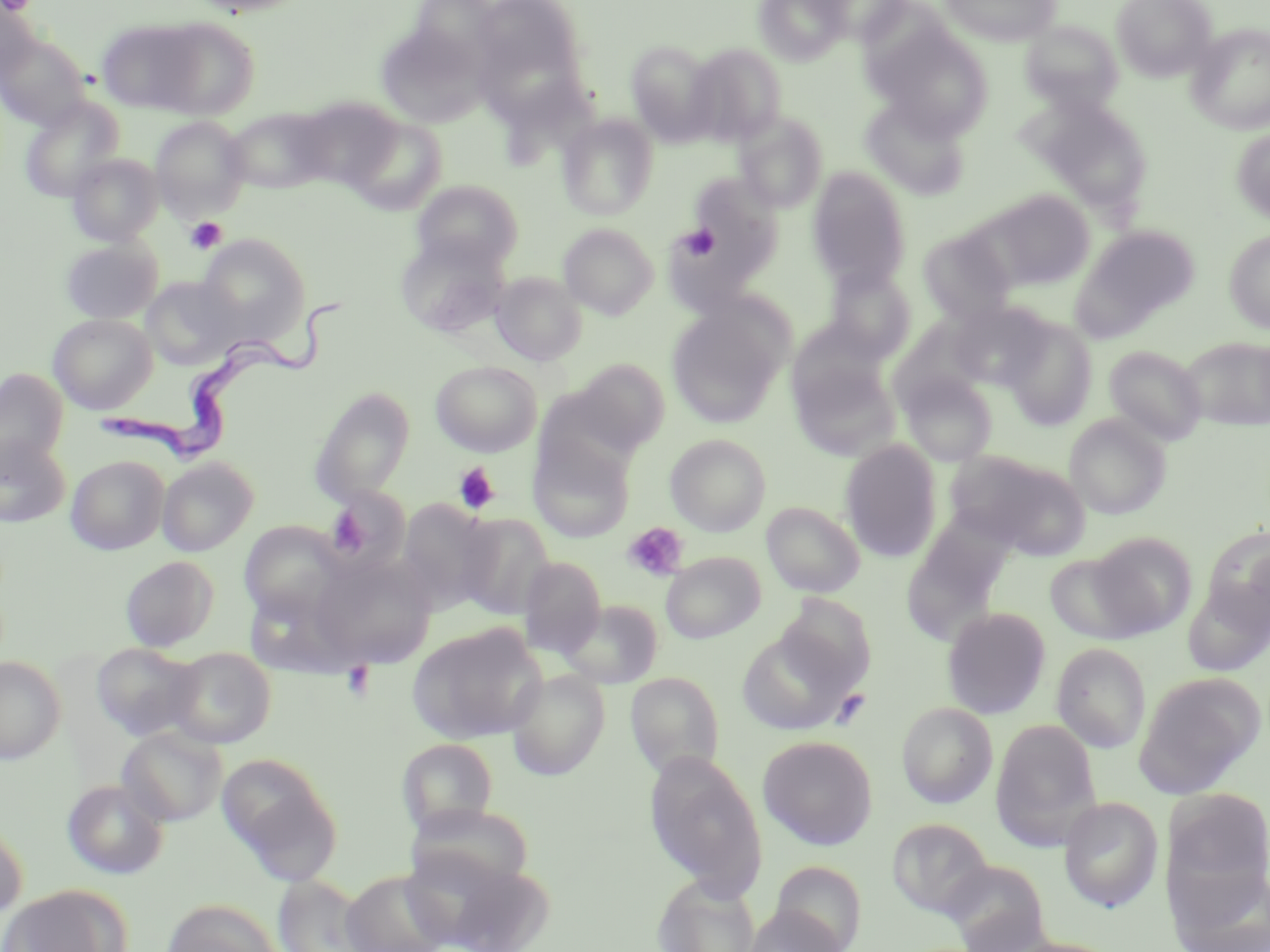

Summary:
  - Coordinate format: approximate bounding boxes as (x1, y1, x2, y2) in pixels
  - Uninfected red blood cell locations: (189, 0, 312, 17), (471, 0, 587, 98), (754, 0, 850, 65), (811, 0, 910, 44), (940, 0, 1062, 46), (1112, 0, 1216, 81), (0, 3, 38, 85), (149, 17, 261, 119), (96, 18, 204, 114), (1021, 20, 1123, 112), (868, 22, 994, 139), (376, 23, 491, 128), (1187, 24, 1270, 134), (0, 31, 90, 129), (626, 40, 720, 146), (685, 43, 787, 146), (292, 96, 401, 190), (860, 96, 971, 199), (19, 97, 124, 201), (1027, 97, 1154, 214), (223, 107, 334, 194), (734, 111, 829, 213), (558, 113, 659, 220), (151, 116, 250, 220), (345, 117, 448, 214), (1231, 128, 1270, 222), (67, 153, 164, 245), (806, 167, 912, 290), (680, 174, 783, 285), (411, 179, 524, 272), (985, 190, 1094, 289), (663, 212, 761, 310), (558, 223, 659, 319), (1072, 225, 1200, 337), (918, 228, 1016, 323), (1224, 229, 1270, 332), (197, 234, 309, 342), (395, 234, 510, 337), (60, 238, 162, 324), (823, 264, 917, 362), (490, 271, 587, 366), (141, 276, 243, 370), (949, 301, 1052, 390), (666, 302, 788, 428), (48, 314, 157, 414), (1003, 317, 1097, 430), (786, 319, 892, 414), (889, 320, 989, 413), (1180, 337, 1270, 431), (1103, 345, 1207, 445), (790, 355, 900, 461), (573, 359, 670, 453), (430, 360, 542, 457), (0, 368, 68, 477), (899, 370, 998, 467), (310, 386, 415, 504), (534, 386, 636, 478), (1064, 414, 1171, 518), (665, 434, 771, 536), (0, 435, 71, 528), (528, 437, 635, 542), (840, 440, 943, 562), (948, 450, 1090, 559), (66, 455, 169, 555), (157, 457, 258, 556), (325, 487, 410, 574), (396, 499, 498, 614), (761, 501, 865, 597), (456, 513, 556, 619), (903, 518, 1012, 638), (240, 522, 345, 621), (1202, 524, 1270, 630), (1086, 531, 1197, 637), (661, 551, 765, 643), (1043, 551, 1153, 644), (120, 555, 219, 652), (309, 555, 436, 669), (518, 556, 607, 658), (1183, 580, 1270, 677), (242, 583, 356, 678), (777, 594, 877, 691), (557, 599, 664, 689), (942, 606, 1051, 719), (408, 622, 546, 744), (736, 627, 857, 736), (1051, 642, 1151, 753), (91, 643, 202, 742), (166, 647, 276, 748), (0, 656, 66, 764), (506, 669, 610, 780), (1134, 671, 1265, 797), (625, 672, 725, 779), (896, 701, 997, 808), (991, 719, 1102, 847), (118, 726, 227, 826), (758, 735, 878, 850), (397, 738, 497, 837), (644, 751, 768, 899), (217, 753, 341, 883), (62, 779, 170, 879), (1163, 787, 1270, 897), (1058, 796, 1163, 912), (887, 817, 993, 918), (0, 822, 28, 924), (428, 856, 554, 952), (942, 859, 1051, 951), (770, 860, 868, 952), (1168, 861, 1270, 952), (340, 869, 452, 952), (272, 875, 379, 952), (652, 876, 762, 952), (0, 884, 131, 952), (160, 898, 282, 952), (740, 905, 848, 952), (999, 936, 1124, 952)
  - Platelet locations: (2, 0, 37, 15), (185, 217, 228, 254), (680, 224, 721, 260), (453, 463, 501, 514), (328, 505, 370, 553), (623, 522, 688, 580), (341, 663, 376, 701)
  - Trypanosoma brucei locations: (94, 295, 345, 461)
  - Slide-level diagnosis: Trypanosoma brucei
  - Preparation: thin blood smear
  - Modality: optical microscopy
  - Field of view: single
  - Image size: 1270×952 pixels
  - Magnification: 1000x
  - Stain: May-Grünwald-Giemsa